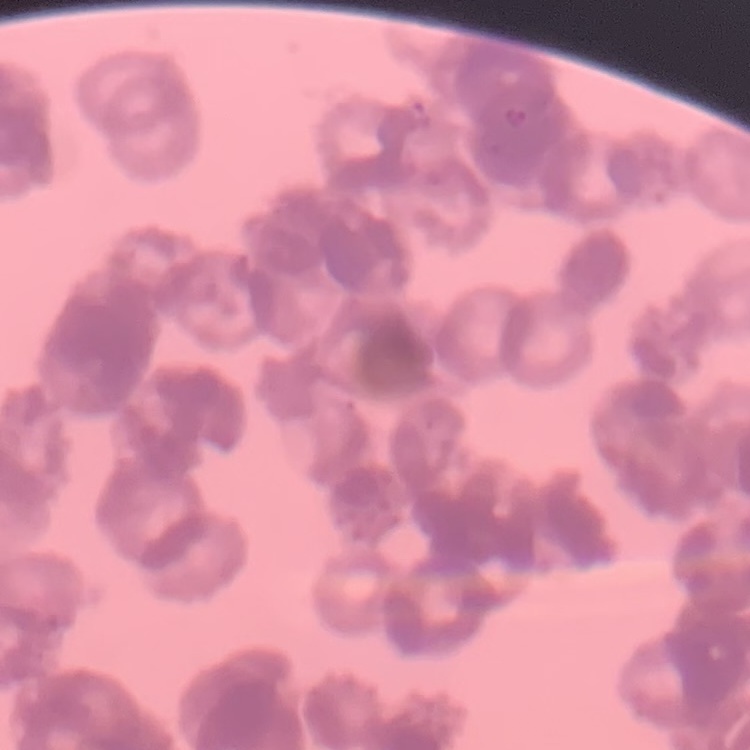
{
  "red_blood_cell_morphology": "rouleaux formation",
  "preparation": "thin blood smear",
  "stain": "Field's or Giemsa",
  "image_type": "one tile cut from a larger photomicrograph"
}